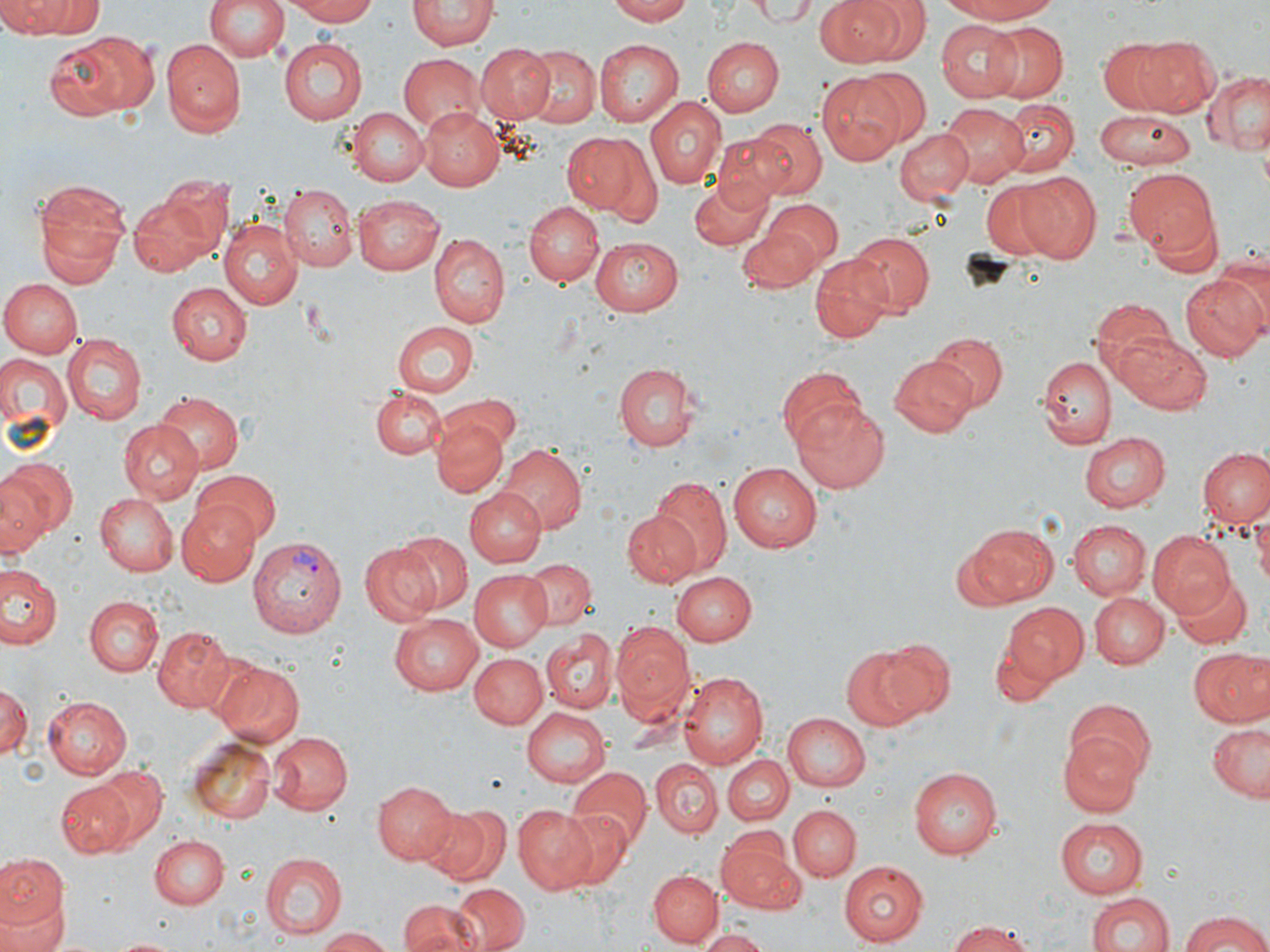

Summary:
  - Coordinate format: approximate bounding boxes as named x1/y1/x2/y2 corners in pixels
  - Uninfected red blood cell locations: (x1=204, y1=0, x2=288, y2=63), (x1=284, y1=0, x2=380, y2=25), (x1=607, y1=0, x2=694, y2=24), (x1=817, y1=0, x2=909, y2=66), (x1=934, y1=0, x2=1063, y2=24), (x1=6, y1=1, x2=101, y2=36), (x1=407, y1=1, x2=497, y2=52), (x1=748, y1=1, x2=824, y2=25), (x1=408, y1=13, x2=495, y2=90), (x1=934, y1=19, x2=1024, y2=103), (x1=981, y1=21, x2=1067, y2=102), (x1=72, y1=31, x2=160, y2=116), (x1=1133, y1=35, x2=1224, y2=117), (x1=701, y1=37, x2=781, y2=116), (x1=1097, y1=38, x2=1183, y2=113), (x1=278, y1=39, x2=368, y2=125), (x1=161, y1=41, x2=242, y2=136), (x1=594, y1=41, x2=683, y2=126), (x1=476, y1=43, x2=555, y2=124), (x1=523, y1=44, x2=599, y2=127), (x1=397, y1=53, x2=482, y2=134), (x1=860, y1=70, x2=931, y2=143), (x1=1201, y1=70, x2=1269, y2=154), (x1=816, y1=72, x2=909, y2=165), (x1=646, y1=96, x2=725, y2=190), (x1=998, y1=98, x2=1078, y2=177), (x1=941, y1=104, x2=1027, y2=187), (x1=418, y1=106, x2=503, y2=191), (x1=346, y1=107, x2=428, y2=185), (x1=1093, y1=109, x2=1195, y2=171), (x1=747, y1=119, x2=826, y2=200), (x1=896, y1=128, x2=973, y2=204), (x1=560, y1=132, x2=651, y2=219), (x1=712, y1=133, x2=798, y2=206), (x1=1123, y1=169, x2=1218, y2=257), (x1=1013, y1=172, x2=1102, y2=262), (x1=687, y1=174, x2=775, y2=250), (x1=31, y1=175, x2=133, y2=285), (x1=978, y1=179, x2=1071, y2=263), (x1=127, y1=184, x2=228, y2=278), (x1=280, y1=185, x2=357, y2=270), (x1=353, y1=194, x2=446, y2=274), (x1=225, y1=196, x2=360, y2=291), (x1=763, y1=199, x2=844, y2=267), (x1=522, y1=201, x2=603, y2=287), (x1=1144, y1=206, x2=1223, y2=279), (x1=218, y1=218, x2=303, y2=310), (x1=738, y1=229, x2=821, y2=293), (x1=847, y1=231, x2=934, y2=315), (x1=429, y1=234, x2=509, y2=329), (x1=588, y1=236, x2=682, y2=315), (x1=809, y1=256, x2=892, y2=343), (x1=1181, y1=273, x2=1269, y2=359), (x1=0, y1=278, x2=80, y2=359), (x1=167, y1=281, x2=252, y2=365), (x1=1089, y1=299, x2=1179, y2=389), (x1=393, y1=321, x2=479, y2=397), (x1=1115, y1=331, x2=1213, y2=415), (x1=928, y1=333, x2=1006, y2=412), (x1=63, y1=334, x2=146, y2=424), (x1=0, y1=355, x2=71, y2=435), (x1=1038, y1=355, x2=1115, y2=449), (x1=888, y1=357, x2=976, y2=437), (x1=613, y1=362, x2=698, y2=452), (x1=776, y1=367, x2=866, y2=452), (x1=368, y1=386, x2=445, y2=459), (x1=153, y1=392, x2=243, y2=473), (x1=439, y1=394, x2=522, y2=455), (x1=792, y1=402, x2=890, y2=493), (x1=431, y1=412, x2=509, y2=498), (x1=118, y1=422, x2=202, y2=505), (x1=1078, y1=432, x2=1169, y2=512), (x1=497, y1=444, x2=588, y2=532), (x1=1198, y1=447, x2=1270, y2=531), (x1=0, y1=456, x2=76, y2=544), (x1=728, y1=464, x2=822, y2=553), (x1=189, y1=467, x2=281, y2=548), (x1=647, y1=477, x2=733, y2=578), (x1=465, y1=490, x2=545, y2=568), (x1=94, y1=492, x2=177, y2=575), (x1=176, y1=501, x2=261, y2=584), (x1=623, y1=509, x2=701, y2=588), (x1=1253, y1=510, x2=1270, y2=596), (x1=1069, y1=520, x2=1149, y2=598), (x1=1077, y1=523, x2=1157, y2=664), (x1=967, y1=524, x2=1059, y2=604), (x1=1147, y1=529, x2=1235, y2=617), (x1=397, y1=531, x2=473, y2=613), (x1=358, y1=541, x2=444, y2=625), (x1=523, y1=556, x2=594, y2=629), (x1=2, y1=563, x2=64, y2=649), (x1=471, y1=568, x2=552, y2=651), (x1=672, y1=571, x2=755, y2=645), (x1=1170, y1=573, x2=1250, y2=648), (x1=1090, y1=593, x2=1168, y2=669), (x1=84, y1=595, x2=162, y2=676), (x1=1002, y1=602, x2=1088, y2=683), (x1=389, y1=614, x2=484, y2=697), (x1=611, y1=621, x2=696, y2=728), (x1=152, y1=625, x2=242, y2=713), (x1=540, y1=628, x2=619, y2=713), (x1=991, y1=635, x2=1059, y2=708), (x1=872, y1=638, x2=956, y2=722), (x1=841, y1=645, x2=931, y2=731), (x1=1188, y1=648, x2=1269, y2=728), (x1=470, y1=653, x2=547, y2=727), (x1=211, y1=658, x2=305, y2=747), (x1=678, y1=673, x2=768, y2=769), (x1=2, y1=683, x2=29, y2=762), (x1=44, y1=696, x2=131, y2=779), (x1=1063, y1=701, x2=1154, y2=783), (x1=520, y1=706, x2=610, y2=788), (x1=781, y1=713, x2=869, y2=791), (x1=1205, y1=724, x2=1270, y2=801), (x1=267, y1=730, x2=351, y2=814), (x1=1059, y1=732, x2=1142, y2=814), (x1=186, y1=735, x2=278, y2=824), (x1=721, y1=756, x2=793, y2=826), (x1=651, y1=759, x2=723, y2=838), (x1=655, y1=760, x2=797, y2=832), (x1=94, y1=766, x2=166, y2=844), (x1=565, y1=767, x2=652, y2=849), (x1=909, y1=768, x2=1001, y2=859), (x1=375, y1=780, x2=457, y2=864), (x1=59, y1=782, x2=133, y2=858), (x1=420, y1=802, x2=509, y2=886), (x1=514, y1=804, x2=602, y2=894), (x1=788, y1=805, x2=862, y2=881), (x1=551, y1=806, x2=637, y2=892), (x1=1055, y1=817, x2=1149, y2=897), (x1=716, y1=829, x2=802, y2=913), (x1=149, y1=835, x2=228, y2=909), (x1=260, y1=853, x2=344, y2=939), (x1=0, y1=855, x2=67, y2=945), (x1=838, y1=860, x2=928, y2=944), (x1=649, y1=871, x2=722, y2=947), (x1=451, y1=883, x2=528, y2=952), (x1=1086, y1=891, x2=1174, y2=952), (x1=0, y1=900, x2=65, y2=952), (x1=398, y1=900, x2=478, y2=952), (x1=1175, y1=911, x2=1270, y2=952), (x1=944, y1=919, x2=1042, y2=952), (x1=314, y1=927, x2=397, y2=951), (x1=697, y1=928, x2=773, y2=952), (x1=109, y1=936, x2=183, y2=952)
  - Plasmodium vivax-infected red blood cell locations: (x1=246, y1=535, x2=345, y2=639)
  - Slide-level diagnosis: Plasmodium vivax
  - Preparation: thin blood smear
  - Modality: light microscopy
  - Field of view: one of a larger specimen
  - Stain: May-Grünwald-Giemsa
  - Image size: 1270×952 pixels
  - Magnification: 1000x